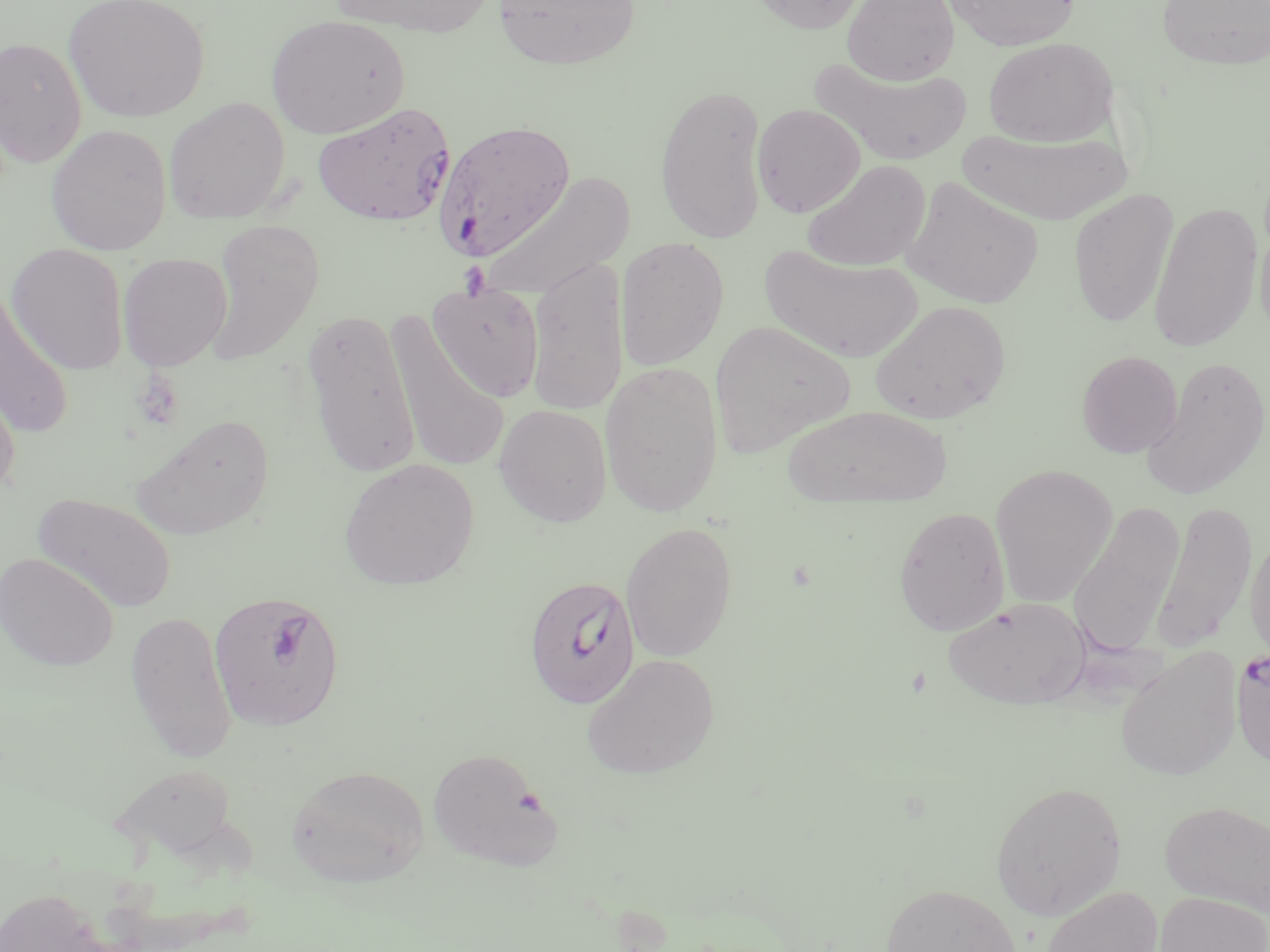

Approximate bounding boxes as named x1/y1/x2/y2 corners in pixels. Plasmodium falciparum-infected red blood cell locations: (x1=313, y1=101, x2=457, y2=226), (x1=435, y1=120, x2=575, y2=260), (x1=523, y1=574, x2=640, y2=710), (x1=208, y1=591, x2=346, y2=731), (x1=1231, y1=646, x2=1270, y2=775). Uninfected red blood cell locations: (x1=62, y1=0, x2=211, y2=123), (x1=326, y1=0, x2=497, y2=37), (x1=491, y1=0, x2=641, y2=70), (x1=746, y1=0, x2=870, y2=34), (x1=842, y1=0, x2=959, y2=85), (x1=940, y1=0, x2=1082, y2=51), (x1=1154, y1=0, x2=1270, y2=71), (x1=266, y1=13, x2=410, y2=139), (x1=1, y1=36, x2=88, y2=167), (x1=984, y1=37, x2=1118, y2=147), (x1=813, y1=59, x2=973, y2=166), (x1=654, y1=82, x2=769, y2=244), (x1=164, y1=97, x2=291, y2=224), (x1=752, y1=103, x2=865, y2=218), (x1=45, y1=124, x2=171, y2=255), (x1=957, y1=128, x2=1135, y2=225), (x1=802, y1=160, x2=931, y2=272), (x1=481, y1=170, x2=634, y2=301), (x1=901, y1=177, x2=1043, y2=310), (x1=1069, y1=188, x2=1178, y2=330), (x1=1148, y1=201, x2=1264, y2=353), (x1=1255, y1=216, x2=1270, y2=345), (x1=205, y1=219, x2=325, y2=365), (x1=615, y1=237, x2=729, y2=371), (x1=5, y1=243, x2=130, y2=375), (x1=760, y1=245, x2=923, y2=363), (x1=117, y1=253, x2=233, y2=370), (x1=526, y1=255, x2=629, y2=417), (x1=1, y1=281, x2=72, y2=438), (x1=428, y1=285, x2=545, y2=402), (x1=870, y1=299, x2=1011, y2=424), (x1=301, y1=308, x2=422, y2=479), (x1=385, y1=312, x2=511, y2=474), (x1=708, y1=319, x2=855, y2=458), (x1=1076, y1=350, x2=1183, y2=458), (x1=1140, y1=356, x2=1270, y2=500), (x1=600, y1=360, x2=724, y2=519), (x1=0, y1=366, x2=22, y2=501), (x1=494, y1=404, x2=613, y2=526), (x1=783, y1=404, x2=952, y2=506), (x1=129, y1=413, x2=275, y2=539), (x1=338, y1=458, x2=480, y2=590), (x1=990, y1=464, x2=1117, y2=607), (x1=31, y1=492, x2=177, y2=615), (x1=1152, y1=500, x2=1258, y2=652), (x1=1068, y1=502, x2=1185, y2=656), (x1=894, y1=505, x2=1011, y2=637), (x1=620, y1=521, x2=738, y2=662), (x1=1245, y1=529, x2=1270, y2=663), (x1=0, y1=553, x2=118, y2=672), (x1=942, y1=596, x2=1091, y2=710), (x1=125, y1=610, x2=238, y2=764), (x1=1115, y1=646, x2=1242, y2=781), (x1=582, y1=653, x2=720, y2=779), (x1=427, y1=747, x2=562, y2=870), (x1=113, y1=763, x2=238, y2=860), (x1=287, y1=765, x2=430, y2=887), (x1=990, y1=780, x2=1127, y2=919), (x1=1160, y1=800, x2=1270, y2=916), (x1=879, y1=882, x2=1021, y2=952), (x1=1040, y1=885, x2=1162, y2=952), (x1=1, y1=887, x2=109, y2=952), (x1=1155, y1=891, x2=1269, y2=952). Slide-level diagnosis: Plasmodium falciparum. 1000x magnification. Image is 1270×952 pixels. Light microscopy. Thin blood smear. One field of a larger specimen. May-Grünwald-Giemsa-stained preparation.